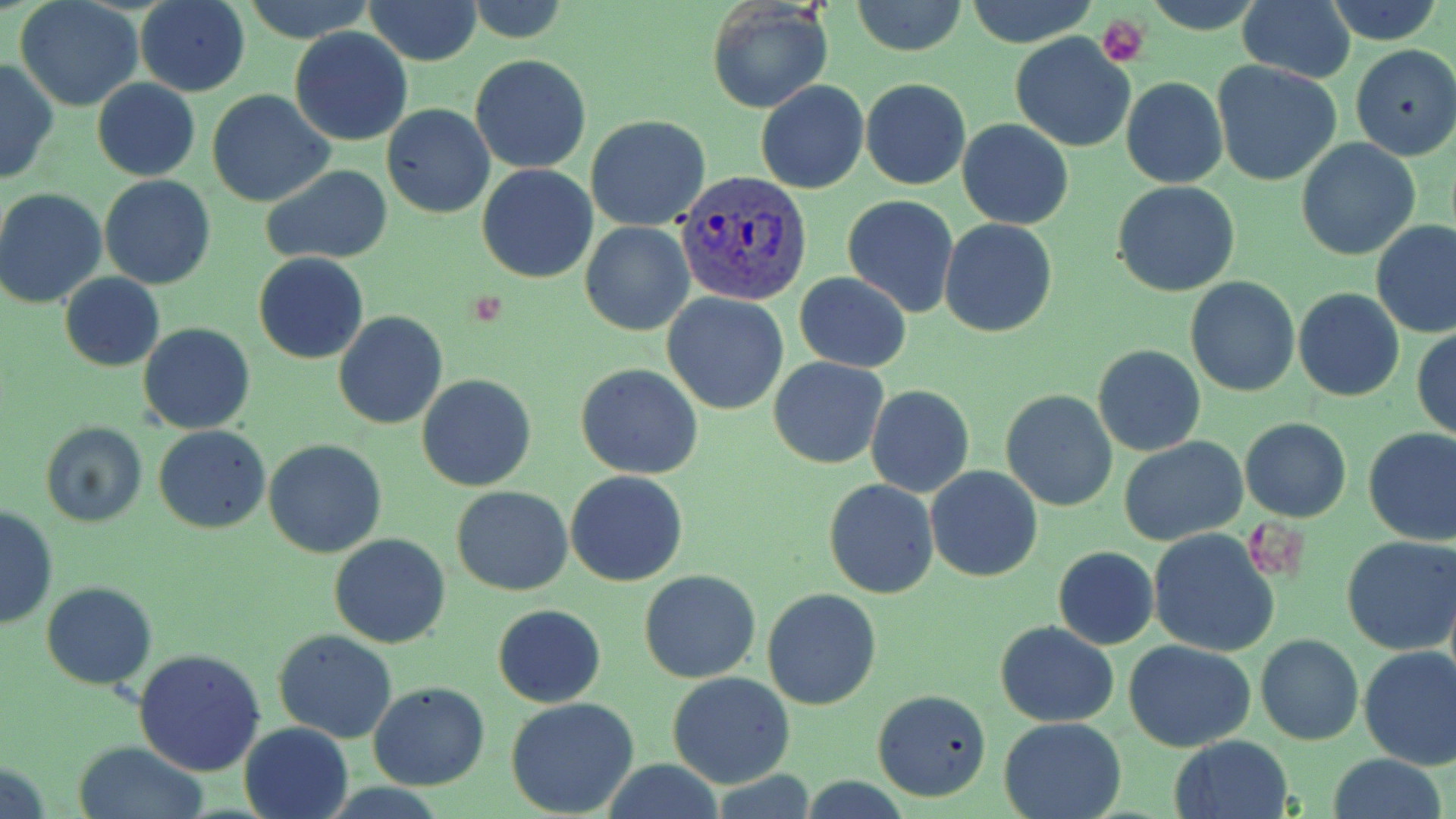 Approximate bounding boxes as (x1, y1, x2, y2) in pixels. Uninfected red blood cell locations: (136, 0, 250, 97), (240, 0, 378, 43), (365, 0, 482, 65), (961, 0, 1101, 48), (1325, 0, 1443, 45), (16, 1, 144, 111), (852, 1, 967, 55), (1237, 1, 1355, 82), (464, 2, 569, 44), (706, 2, 833, 114), (291, 28, 412, 147), (1011, 33, 1137, 152), (1350, 44, 1456, 161), (470, 55, 591, 174), (0, 58, 58, 186), (1212, 60, 1344, 188), (1121, 77, 1228, 188), (861, 79, 970, 189), (93, 80, 200, 181), (756, 81, 869, 193), (207, 90, 334, 208), (382, 104, 495, 218), (585, 115, 711, 230), (957, 120, 1074, 230), (1296, 139, 1421, 260), (261, 164, 394, 264), (478, 164, 597, 283), (99, 176, 216, 290), (1111, 180, 1241, 296), (0, 188, 108, 308), (843, 194, 960, 318), (938, 219, 1058, 338), (580, 220, 695, 336), (1371, 220, 1456, 338), (254, 253, 369, 364), (795, 272, 911, 372), (60, 273, 164, 372), (1184, 275, 1300, 398), (1294, 288, 1404, 401), (662, 293, 789, 414), (334, 310, 448, 429), (138, 322, 255, 434), (1412, 328, 1456, 441), (1093, 345, 1207, 458), (770, 358, 889, 469), (576, 365, 703, 479), (418, 374, 535, 491), (865, 384, 975, 498), (1001, 389, 1118, 510), (1240, 418, 1352, 522), (41, 421, 149, 528), (154, 425, 270, 533), (1362, 428, 1456, 546), (1120, 438, 1248, 547), (264, 439, 386, 557), (925, 466, 1043, 582), (564, 470, 688, 586), (824, 480, 938, 599), (452, 486, 572, 595), (1, 506, 58, 630), (1148, 528, 1280, 656), (328, 533, 451, 648), (1342, 536, 1456, 655), (1053, 546, 1159, 649), (640, 569, 761, 683), (41, 581, 156, 690), (762, 589, 884, 710), (495, 604, 606, 707), (995, 621, 1120, 726), (274, 630, 398, 743), (1256, 634, 1363, 744), (1124, 640, 1256, 751), (1359, 646, 1456, 770), (135, 647, 267, 776), (668, 672, 796, 790), (368, 682, 490, 789), (872, 689, 993, 802), (505, 698, 641, 819), (998, 716, 1130, 819), (239, 721, 354, 819), (1168, 736, 1294, 819), (72, 741, 210, 819), (1328, 754, 1448, 819), (601, 759, 726, 819), (711, 770, 816, 817), (795, 776, 917, 816). Plasmodium vivax-infected red blood cell locations: (672, 166, 808, 303). Platelet locations: (1098, 16, 1148, 67), (1243, 515, 1308, 586). Slide-level diagnosis: Plasmodium vivax. Light microscopy. Thin blood film. One field of a larger specimen. 1000x magnification. Image is 1456×819 pixels. May-Grünwald-Giemsa-stained preparation.